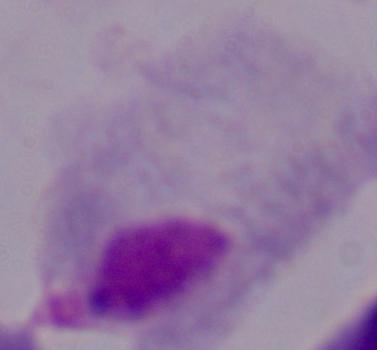
modality = photomicrograph
magnification = 1000x
identification = trichomonad